Classify this cell by malaria status.
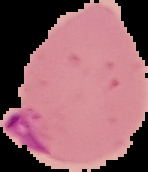

It is parasitized.

image_type: segmented cell region with the area outside set to black
image_size: 148×172 pixels
preparation: thin blood film